Locate every Plasmodium malariae-infected red blood cell.
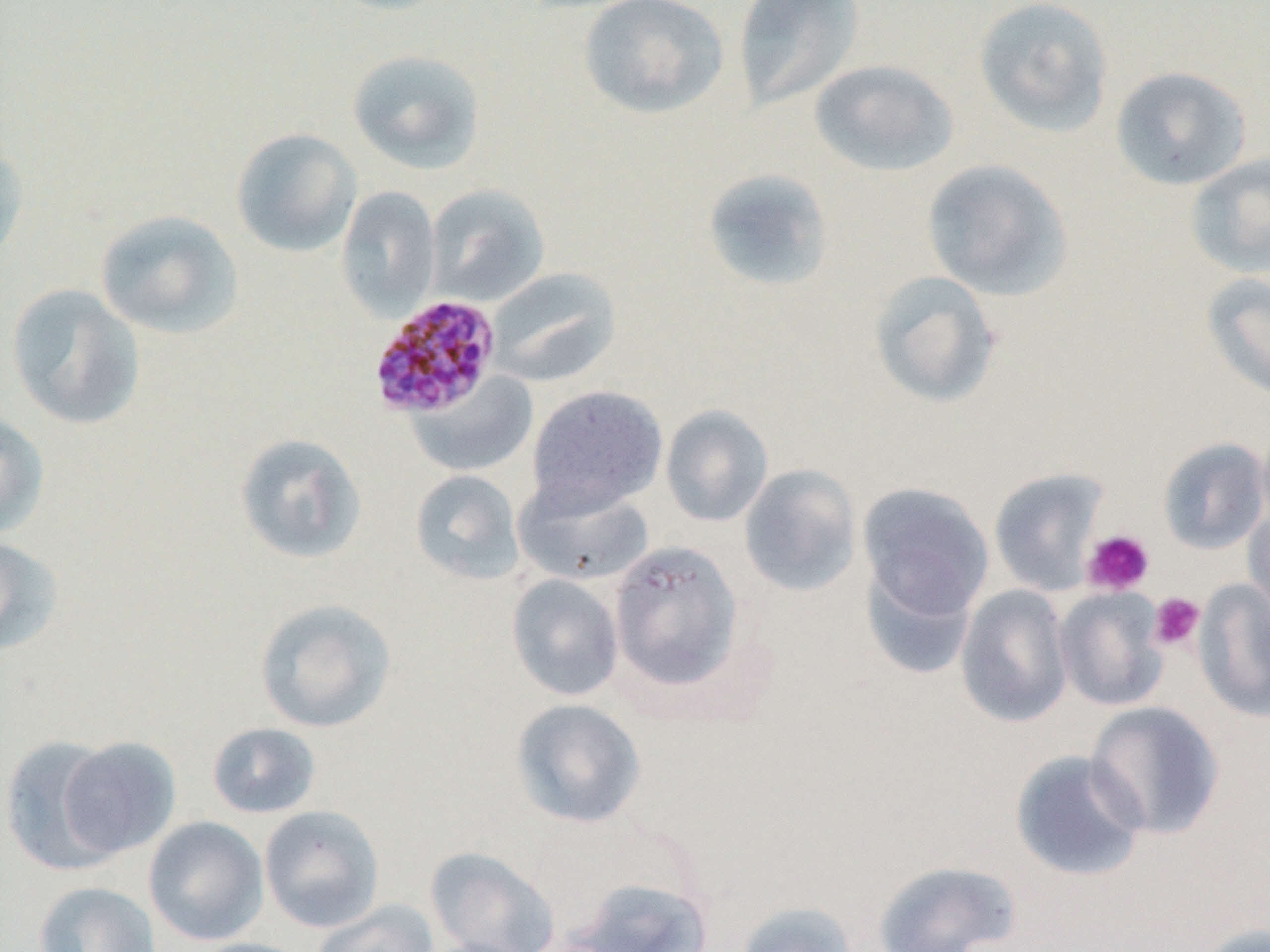

Approximate bounding boxes as (x1, y1, x2, y2) in pixels.
Plasmodium malariae-infected red blood cells: (368, 294, 503, 420).

{
  "slide_level_diagnosis": "Plasmodium malariae",
  "modality": "light microscopy",
  "platelet_locations": "approximate bounding boxes as (x1, y1, x2, y2) in pixels: (1082, 529, 1155, 596), (1148, 592, 1205, 651)",
  "uninfected_red_blood_cell_locations": "approximate bounding boxes as (x1, y1, x2, y2) in pixels: (732, 0, 865, 113), (973, 0, 1115, 138), (578, 1, 729, 119), (347, 48, 486, 175), (809, 59, 960, 177), (1110, 66, 1252, 191), (231, 127, 362, 258), (0, 140, 30, 268), (1185, 151, 1270, 280), (921, 158, 1073, 302), (701, 168, 835, 293), (426, 184, 549, 307), (337, 187, 441, 319), (95, 209, 244, 340), (487, 267, 621, 387), (867, 270, 1003, 409), (1201, 271, 1270, 403), (6, 283, 145, 430), (406, 370, 538, 478), (526, 385, 668, 515), (660, 404, 773, 527), (0, 408, 50, 539), (1256, 419, 1270, 533), (234, 432, 367, 565), (1157, 437, 1269, 555), (738, 463, 863, 598), (988, 467, 1110, 596), (409, 469, 525, 585), (512, 478, 656, 587), (857, 482, 994, 623), (1243, 506, 1270, 624), (0, 535, 64, 657), (608, 539, 747, 697), (858, 559, 980, 680), (506, 573, 624, 701), (1193, 578, 1270, 724), (955, 584, 1074, 728), (1053, 586, 1169, 712), (253, 597, 398, 734), (510, 698, 646, 829), (1085, 701, 1226, 840), (207, 722, 322, 819), (0, 735, 125, 874), (56, 736, 181, 859), (1009, 749, 1148, 883), (258, 805, 385, 933), (143, 816, 269, 946), (425, 846, 561, 952), (872, 859, 1021, 952), (567, 875, 714, 951), (33, 881, 161, 952), (311, 899, 440, 952), (733, 901, 860, 952), (1193, 922, 1270, 952), (186, 938, 316, 952)",
  "magnification": "1000x",
  "image_size": "1270×952 pixels",
  "preparation": "thin blood film",
  "field_of_view": "single"
}